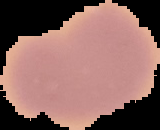

Summary:
  - Image type: cell region segmented out of the field of view; surrounding area masked to black
  - Preparation: thin blood film
  - Image size: 160×130 pixels
  - Result: negative for Plasmodium parasites